Point out each Plasmodium parasite.
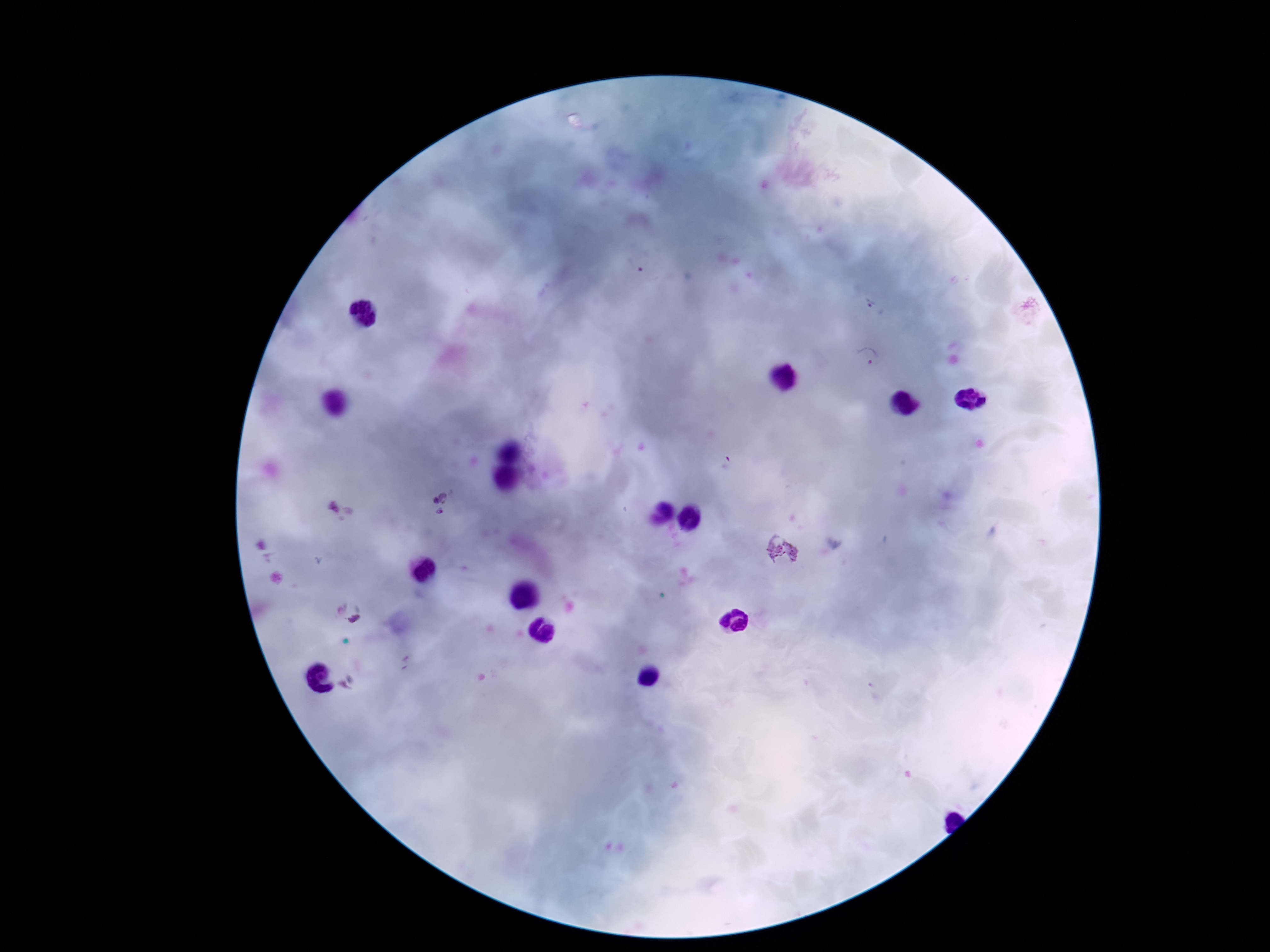
Approximate centers as (x, y) in pixels.
Plasmodium parasites: (636, 267), (876, 309), (866, 360), (439, 504), (779, 553), (356, 621).

Summary:
  - Stain: Giemsa
  - Capture: smartphone camera through the microscope eyepiece
  - Field of view: single
  - Magnification: 100x
  - Image size: 1270×952 pixels
  - Patient malaria status: positive
  - Preparation: thick blood smear